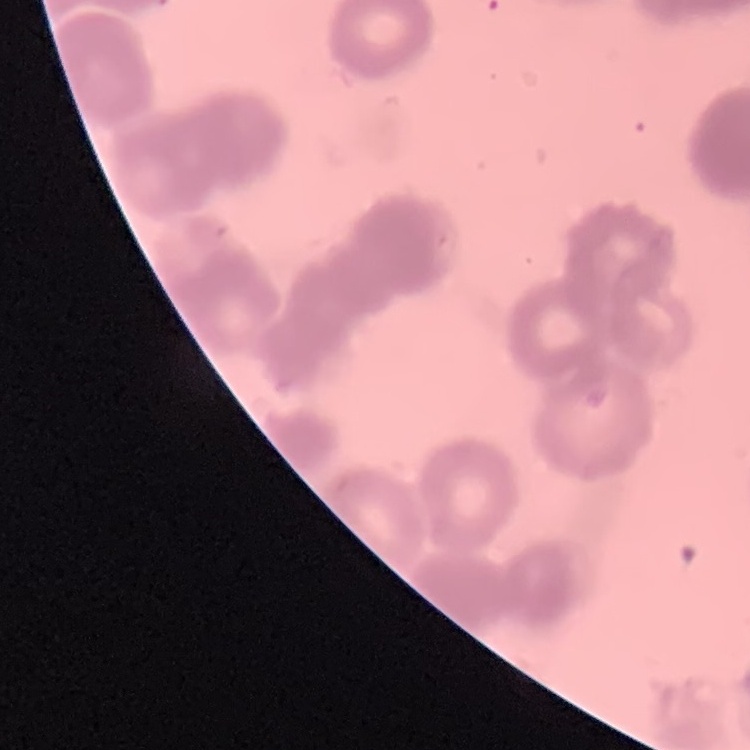
{
  "erythrocyte_morphology": "rouleaux formation",
  "stain": "Field's or Giemsa",
  "preparation": "thin peripheral smear",
  "image_type": "square crop of a larger photomicrograph"
}